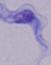

1000x magnification. Photomicrograph. A trypanosome is seen.